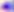

modality: micrograph
identification: Toxoplasma gondii
magnification: 400x